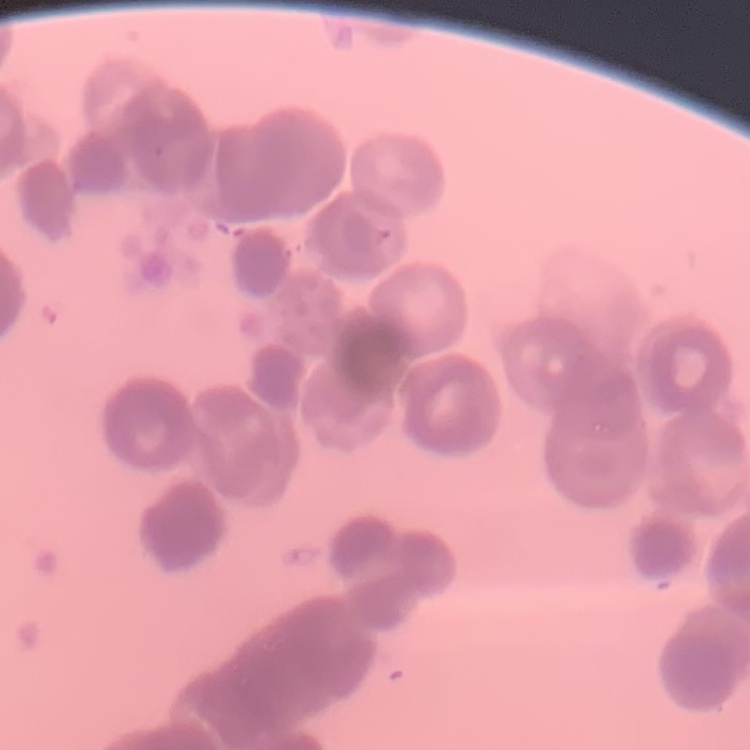
{
  "erythrocyte_morphology": "rouleaux formation",
  "image_type": "square crop of a larger photomicrograph",
  "stain": "Field's or Giemsa",
  "preparation": "thin peripheral smear"
}